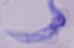
Summary:
  - Modality: photomicrograph
  - Identification: trypanosome
  - Magnification: 1000x